State which parasite is depicted.
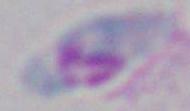
Toxoplasma gondii.

Captured at 1000x magnification. Photomicrograph.